Assess this cell for malaria.
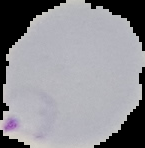

Parasitized.

{
  "preparation": "thin blood film",
  "image_size": "145×148 pixels",
  "image_type": "segmented cell region on a black background"
}